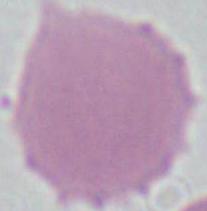
Summary:
  - Identification: red blood cell
  - Modality: photomicrograph
  - Magnification: 1000x